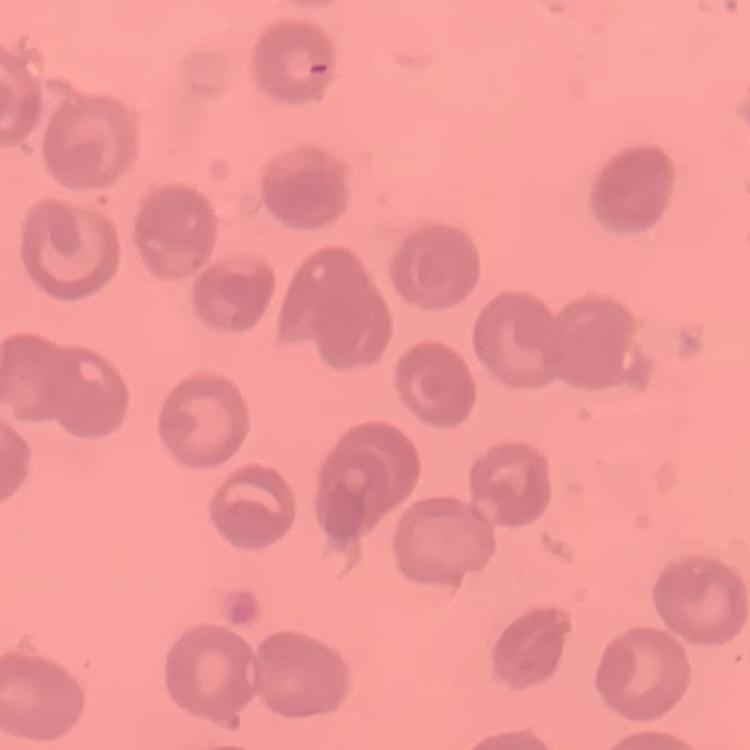

Summary:
  - Red blood cell morphology: no rouleaux formation
  - Stain: Field's or Giemsa
  - Preparation: thin blood film
  - Image type: square crop of a larger photomicrograph